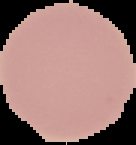 The area outside the segmented cell region is set to black. From a thin blood film. Image is 136×145 pixels. Result: no malaria parasites seen.